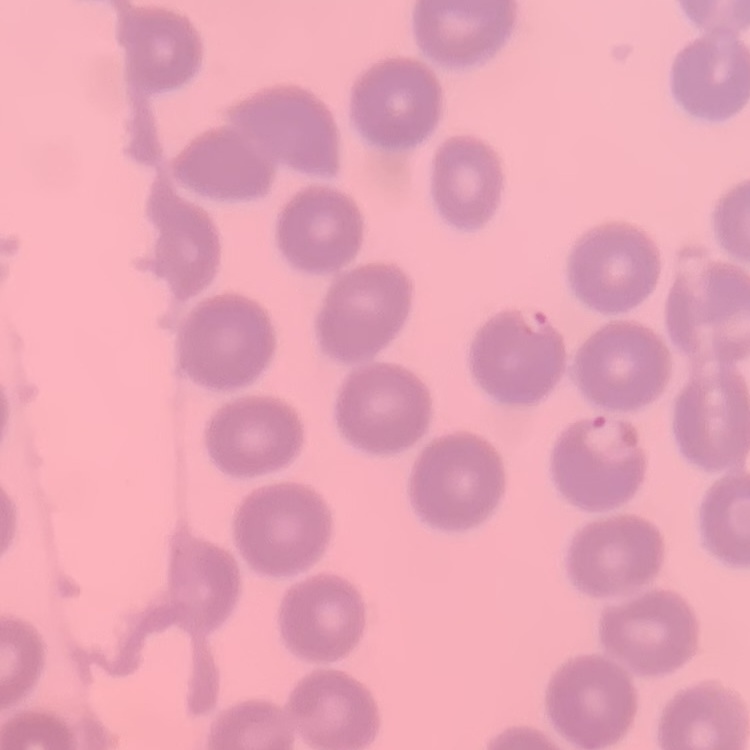 The red blood cells show no rouleaux formation. Square crop of a larger photomicrograph. Stained with either Field's or Giemsa. Thin blood film.